Name the cell type shown.
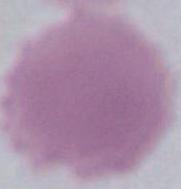
This is an erythrocyte.

{
  "modality": "photomicrograph",
  "magnification": "1000x"
}